Classify the preparation.
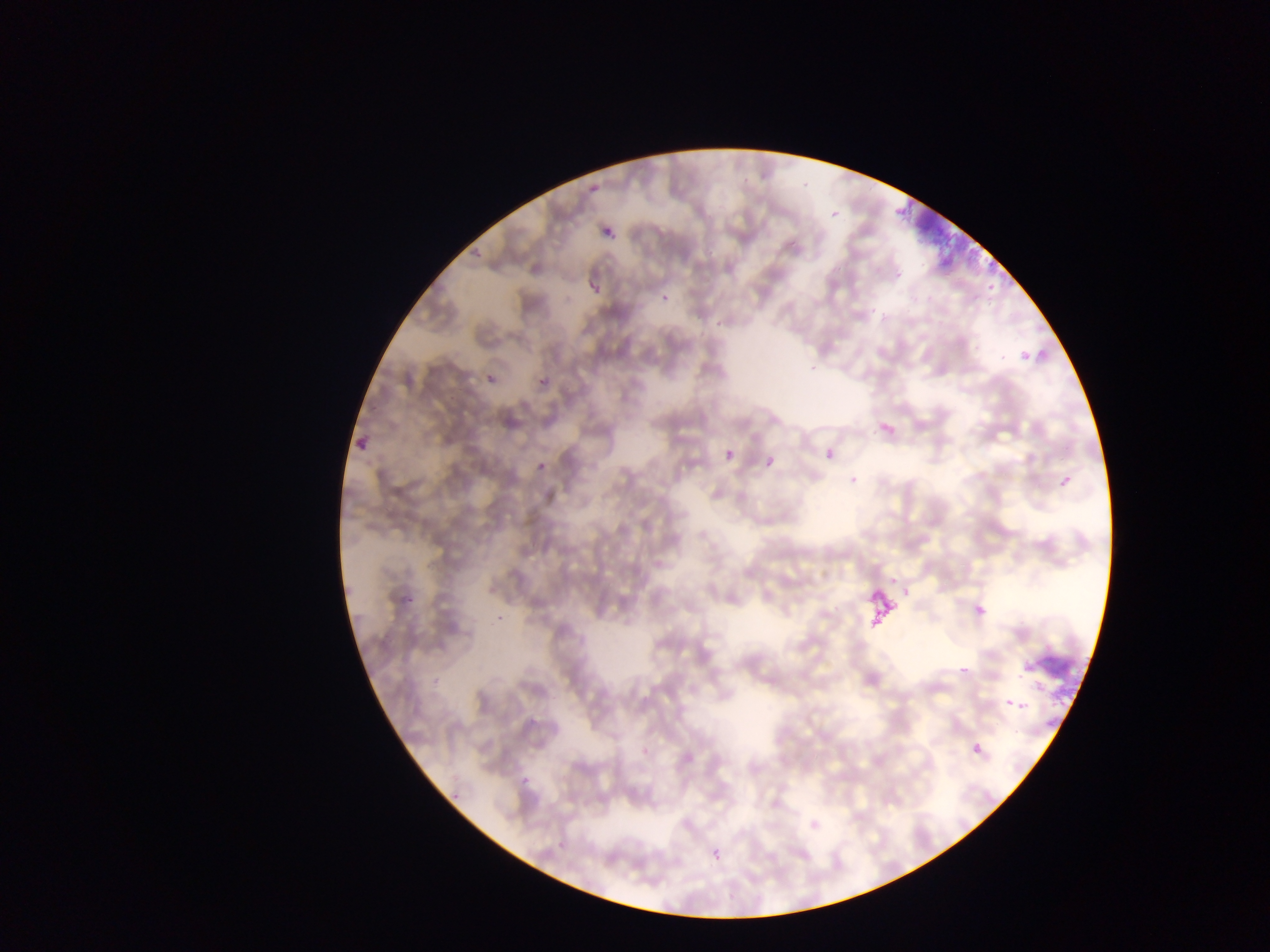

This is a thin smear.

{
  "plasmodium_parasite_locations": "approximate bounding boxes as (left, top, right, bottom) in pixels: (829, 207, 843, 222), (603, 226, 616, 240), (588, 280, 604, 299), (536, 376, 550, 391), (873, 414, 903, 446), (822, 444, 840, 464), (723, 448, 737, 464), (761, 452, 782, 476), (1057, 471, 1077, 494), (968, 596, 992, 624), (1006, 697, 1029, 714), (969, 739, 989, 763)",
  "capture": "mobile-phone photograph through a microscope",
  "field_of_view": "single",
  "country": "Ghana",
  "artifact_stain_precipitate_or_debris_locations": "approximate bounding boxes as (left, top, right, bottom) in pixels: (900, 192, 994, 283), (858, 564, 903, 633), (1019, 630, 1087, 703)",
  "image_size": "1270×952 pixels"
}